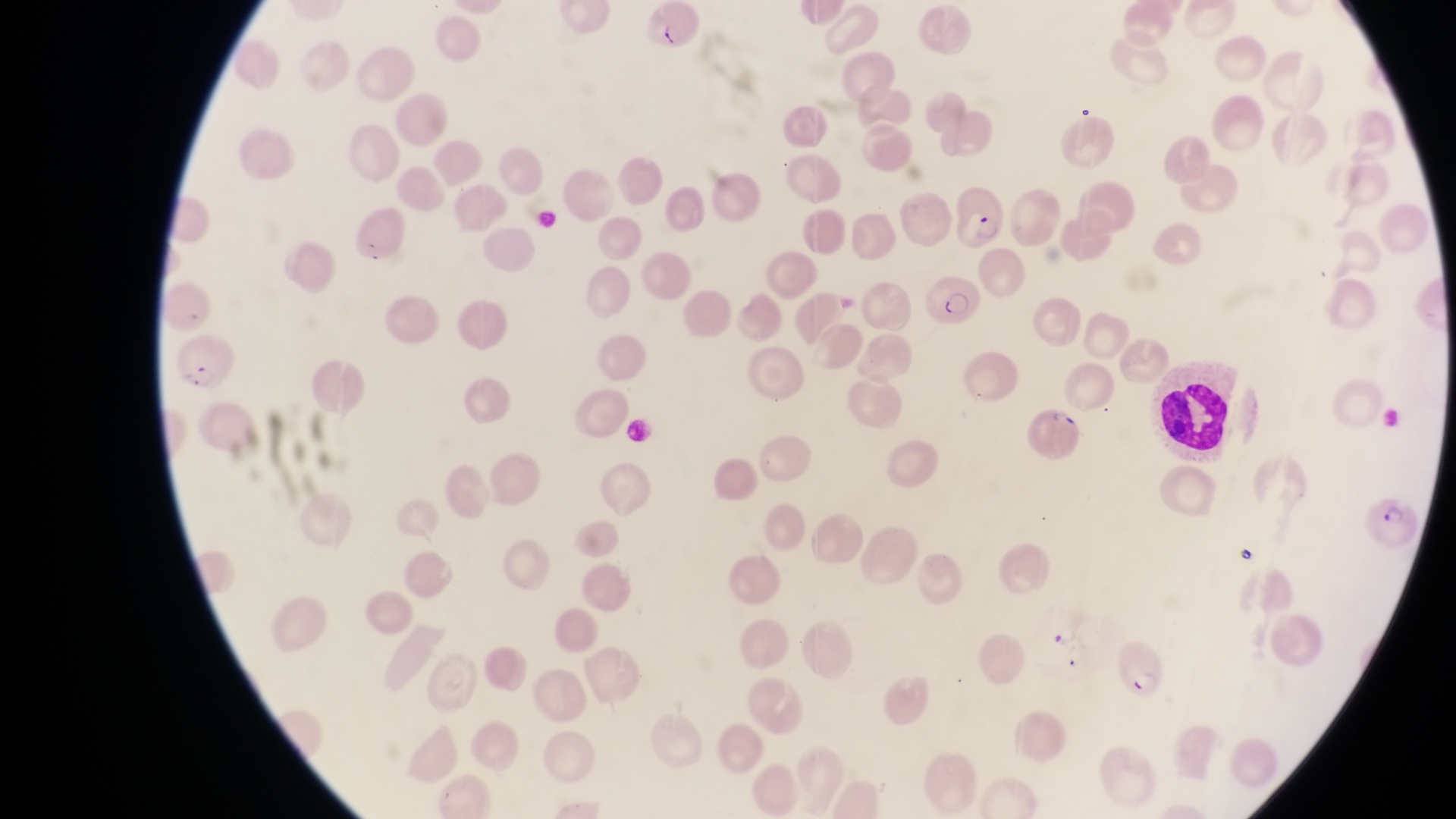
Approximate bounding boxes as {left, top, right, bottom} in pixels.
Summary:
  - Leukocyte locations: {1159, 375, 1227, 447}
  - Parasitised red blood cell locations: {954, 182, 1009, 253}, {927, 271, 985, 329}, {171, 334, 242, 398}, {1028, 404, 1086, 463}, {1369, 495, 1425, 556}, {1115, 635, 1175, 698}
  - Magnification: 1000x
  - Image size: 1456×819 pixels
  - Field of view: single
  - Country: Uganda
  - Capture: smartphone photograph through the eyepiece of an Olympus CX-23 microscope
  - Preparation: thin blood smear